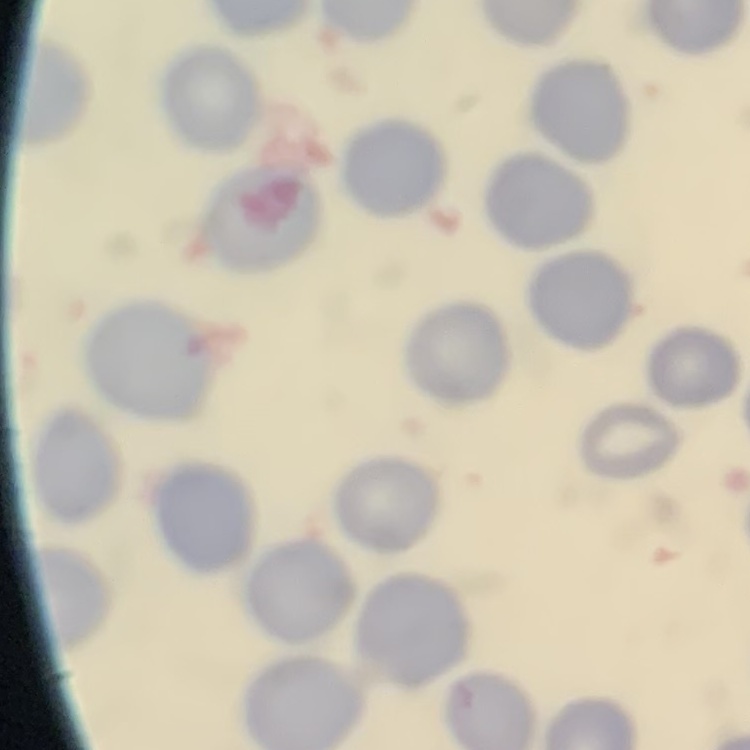
{
  "red_blood_cell_morphology": "no rouleaux formation",
  "preparation": "thin blood film",
  "image_type": "square crop of a larger photomicrograph",
  "stain": "Field's or Giemsa"
}